Locate every Plasmodium parasite.
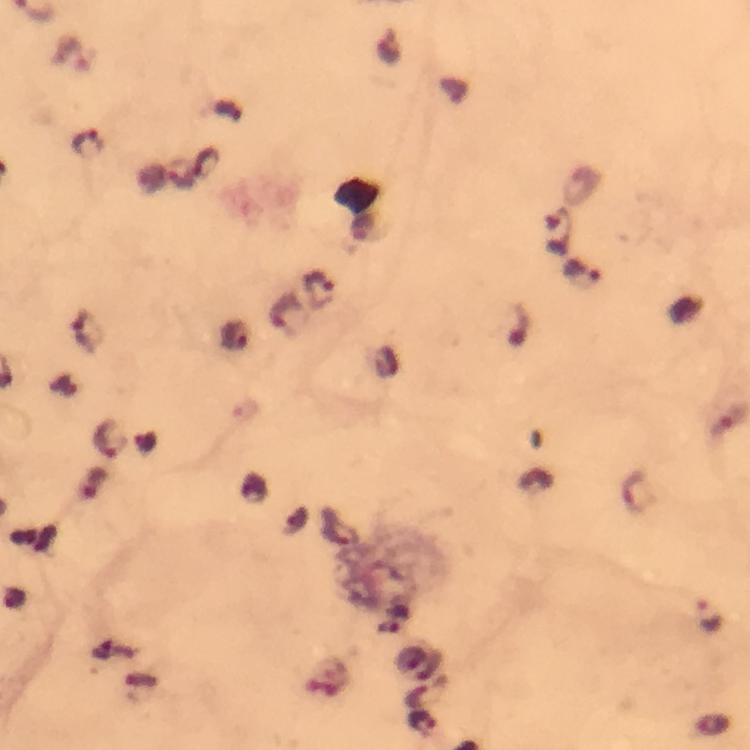

Approximate centers as {x, y} in pixels.
Plasmodium parasites: {87, 142}, {207, 164}, {182, 174}, {559, 231}, {583, 273}, {319, 290}, {87, 333}, {729, 420}, {109, 438}, {634, 490}, {709, 617}, {424, 692}, {422, 723}.

capture = smartphone mounted on the microscope
stain = Giemsa
preparation = thick blood smear
magnification = 100x
image size = 750×750 pixels
cropped from = one field of view
immersion oil = used
context = from a malaria diagnostic workup